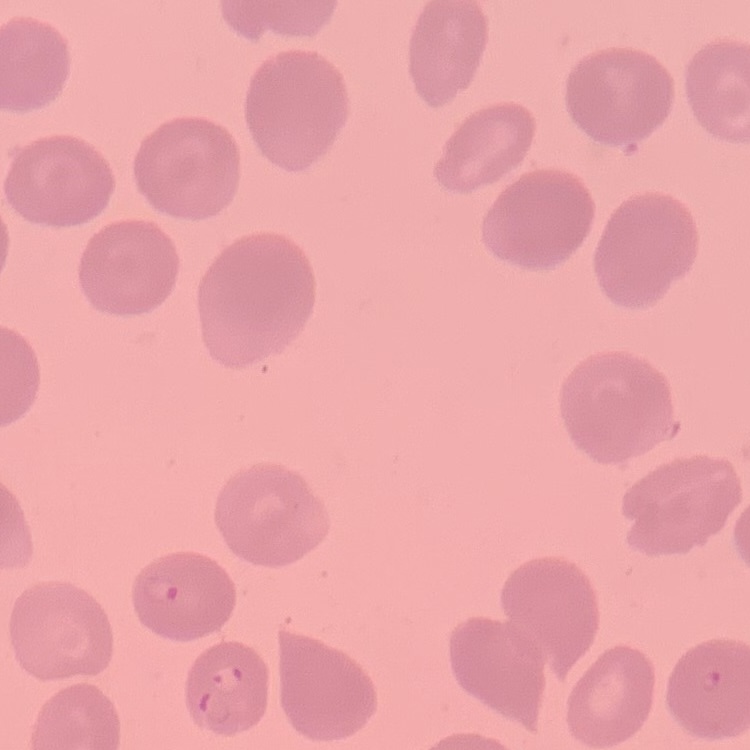
The erythrocytes exhibit no rouleaux formation. Thin peripheral smear. Stained with either Field's or Giemsa. Square crop of a larger photomicrograph.